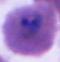

{
  "modality": "photomicrograph",
  "magnification": "400x or 1000x",
  "identification": "Plasmodium"
}